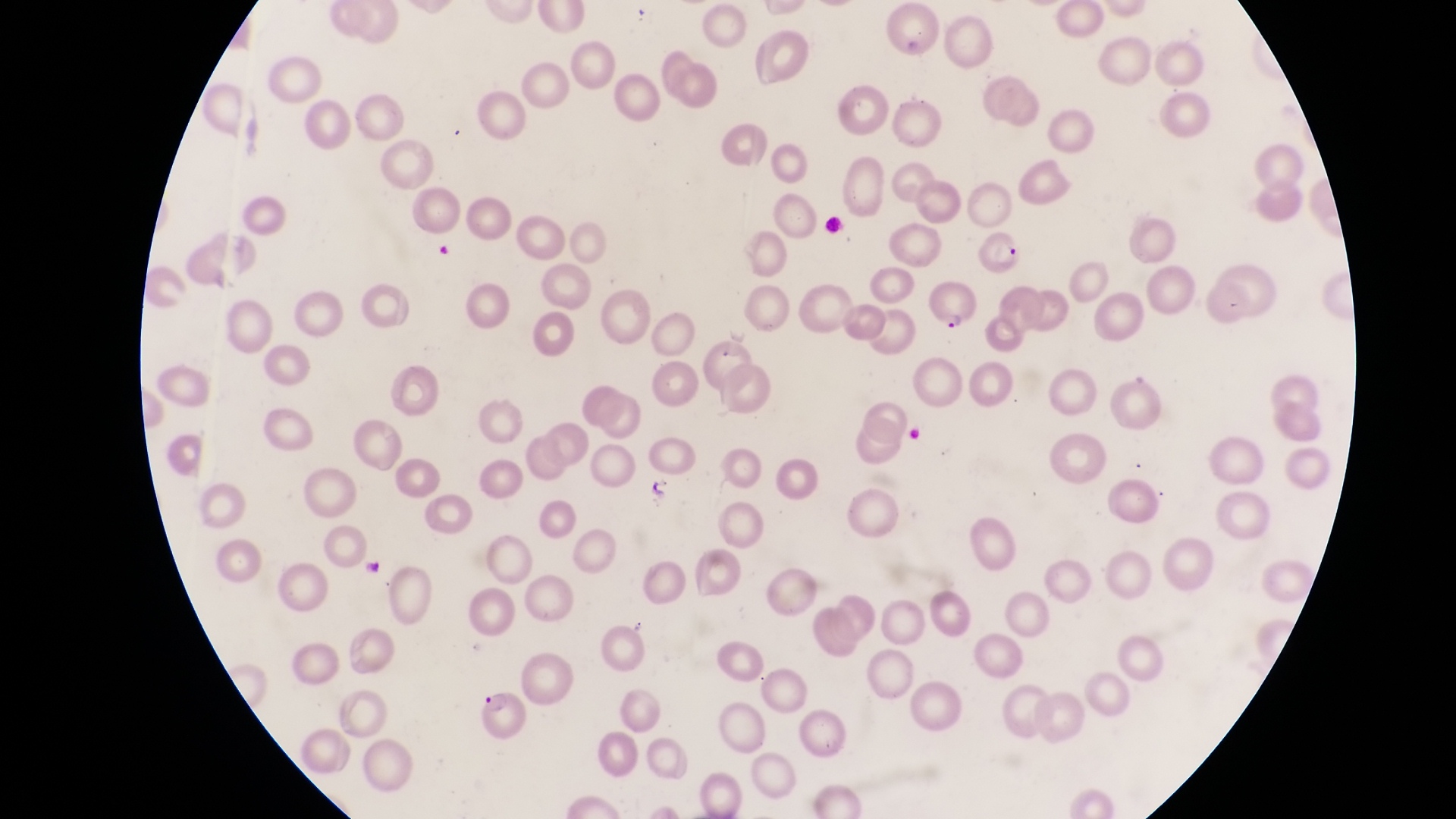

Approximate bounding boxes as (left, top, right, bottom) in pixels.
Summary:
  - Artifact (platelet-like body, stain precipitate, or debris) locations: (644, 476, 676, 503)
  - Parasitised red blood cell locations: (970, 227, 1023, 285), (925, 281, 980, 336), (698, 336, 753, 397), (476, 689, 531, 748)
  - Country: Uganda
  - Image size: 1456×819 pixels
  - Preparation: thin blood film
  - Field of view: single
  - Magnification: 1000x
  - Capture: smartphone photograph through the eyepiece of an Olympus CX-23 microscope